Assess the morphology of the red blood cells.
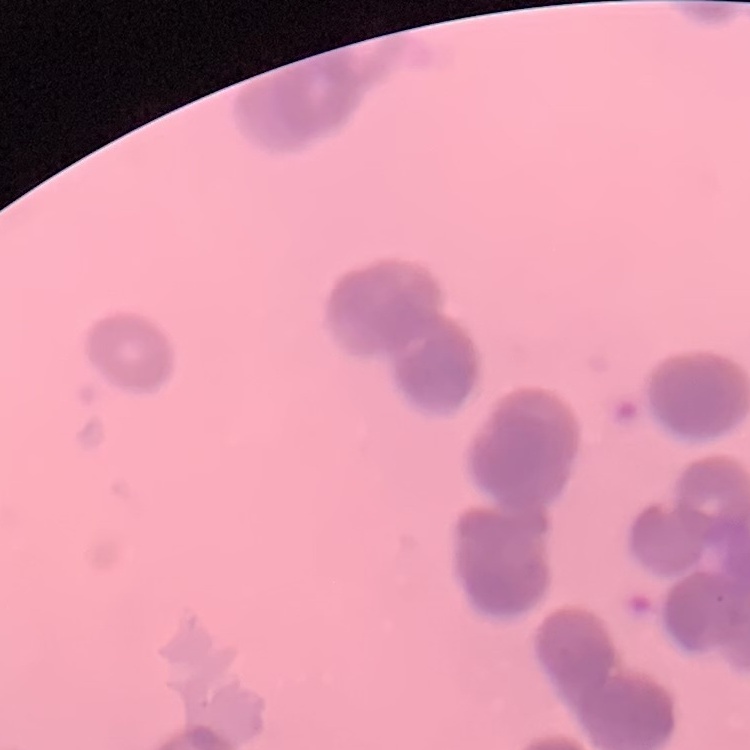

Rouleaux formation.

stain = Field's or Giemsa
image type = one tile cut from a larger photomicrograph
preparation = thin peripheral smear